Assess this cell for malaria.
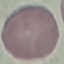
Uninfected.

stain = Giemsa
image type = cell patch, automatically extracted from a larger field of view and resized to 64 × 64 pixels
preparation = thin smear
capture = smartphone through the microscope eyepiece